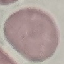

Result: negative for malaria parasites. Giemsa-stained preparation. Cell patch, automatically extracted from a larger field of view and resized to 64 × 64 pixels. Thin blood film. Photographed with a smartphone camera at the microscope eyepiece.